Give the preparation type.
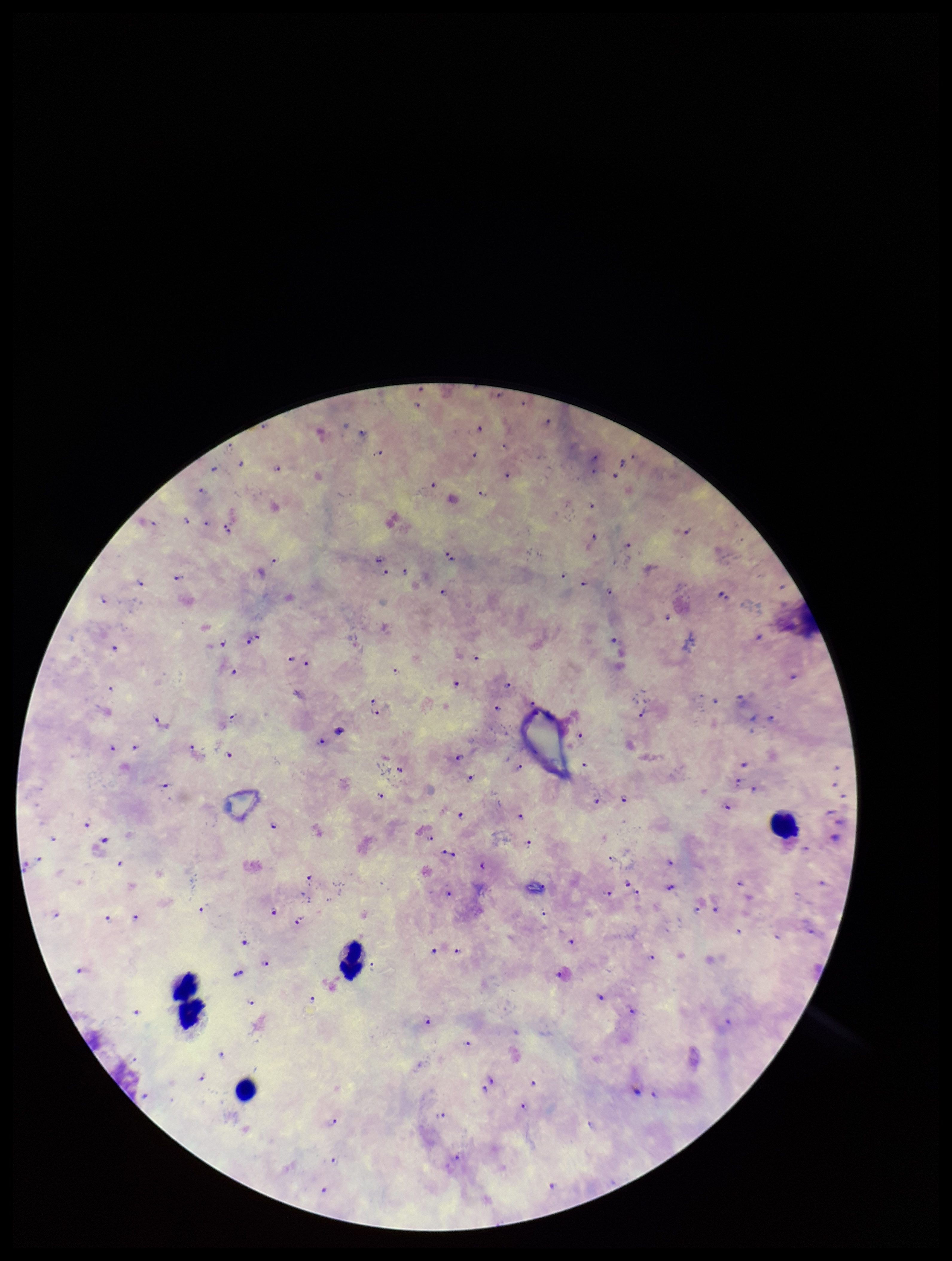

A thick smear.

Summary:
  - Stain: Giemsa
  - Field of view: one from this slide
  - Leukocyte count: 5
  - Patient malaria status: infected
  - Species reported for this patient: Plasmodium falciparum
  - Plasmodium parasites: identified
  - Parasite count: 110
  - Capture: smartphone photograph through the microscope eyepiece
  - Image size: 952×1261 pixels